Outline each white blood cell.
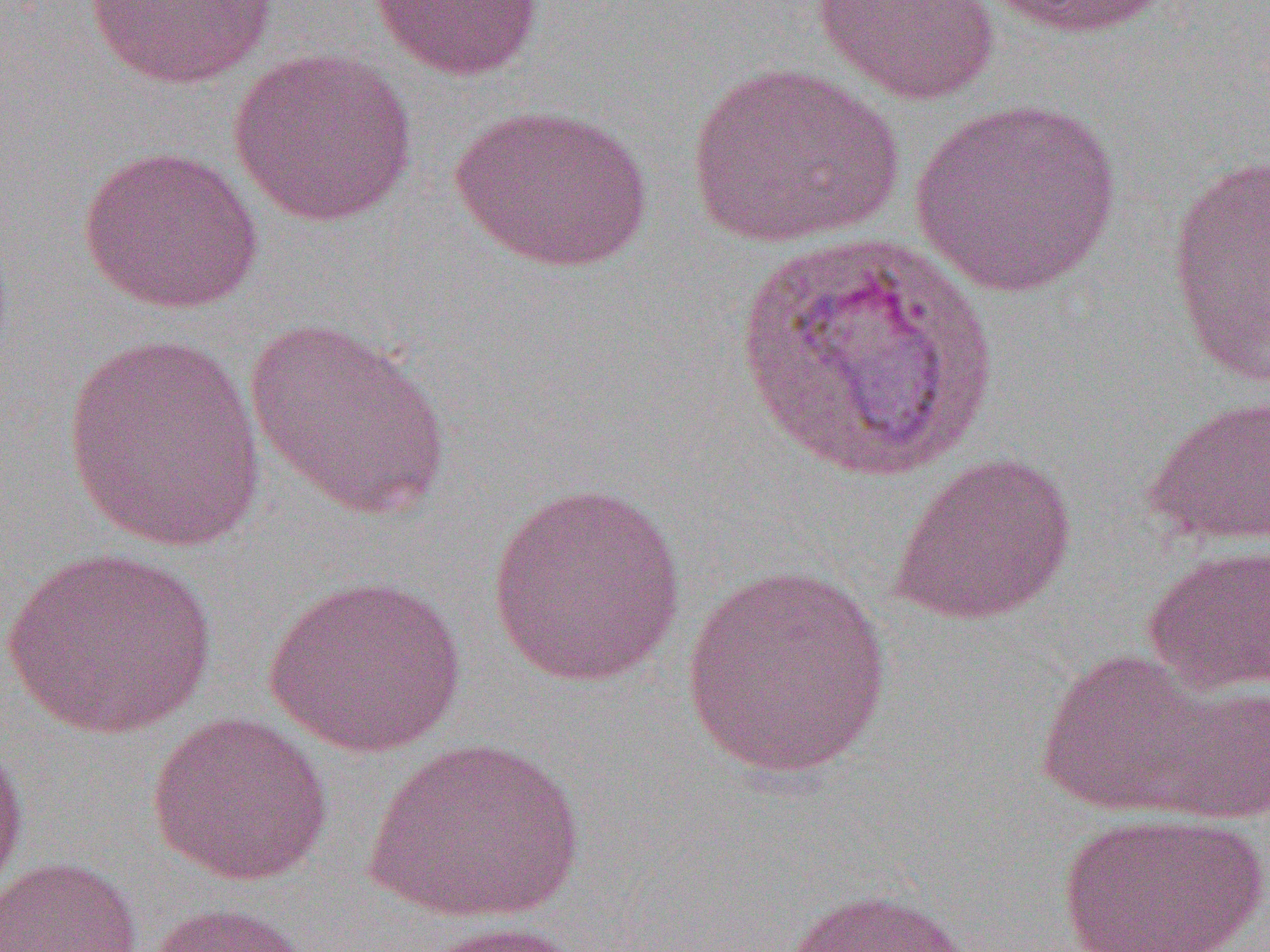
Approximate bounding boxes as (x1,y1)-(x2,y2) corner pairs in pixels.
White blood cells: (729,231)-(1006,488).

Uninfected red blood cell locations: (83,0)-(280,88), (369,0)-(545,82), (979,0)-(1175,39), (809,1)-(1003,106), (228,48)-(418,227), (685,61)-(905,249), (909,97)-(1124,298), (449,103)-(654,274), (78,144)-(265,314), (1166,153)-(1270,387), (243,317)-(452,520), (60,333)-(269,554), (1142,393)-(1270,548), (887,450)-(1078,626), (487,480)-(687,688), (1140,543)-(1270,696), (1,547)-(219,739), (679,565)-(895,781), (262,575)-(468,758), (1034,647)-(1239,820), (1138,677)-(1270,825), (148,711)-(335,885), (0,729)-(31,904), (364,734)-(584,925), (1055,810)-(1269,952), (0,856)-(144,952), (784,886)-(986,952), (145,901)-(314,952), (410,920)-(591,952). Slide-level diagnosis: Plasmodium vivax. Light microscopy. One field of a larger specimen. Thin blood smear. Image is 1270×952 pixels. 1000x magnification.